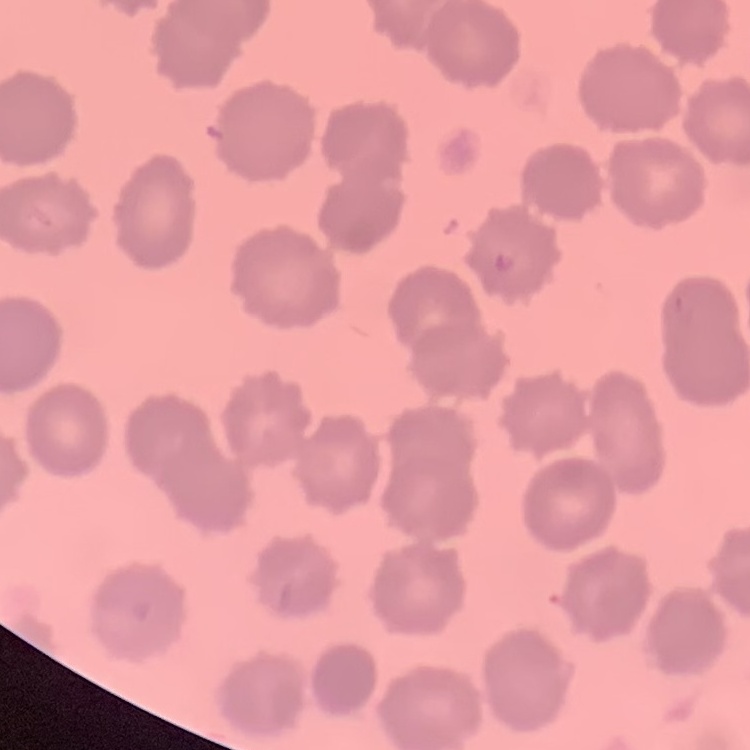
{
  "erythrocyte_morphology": "no rouleaux formation",
  "image_type": "one tile cut from a larger photomicrograph",
  "preparation": "thin blood smear",
  "stain": "Field's or Giemsa"
}